Name the cell type shown.
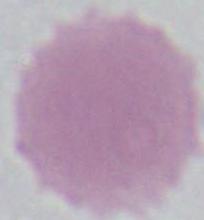
An erythrocyte.

1000x magnification. Photomicrograph.